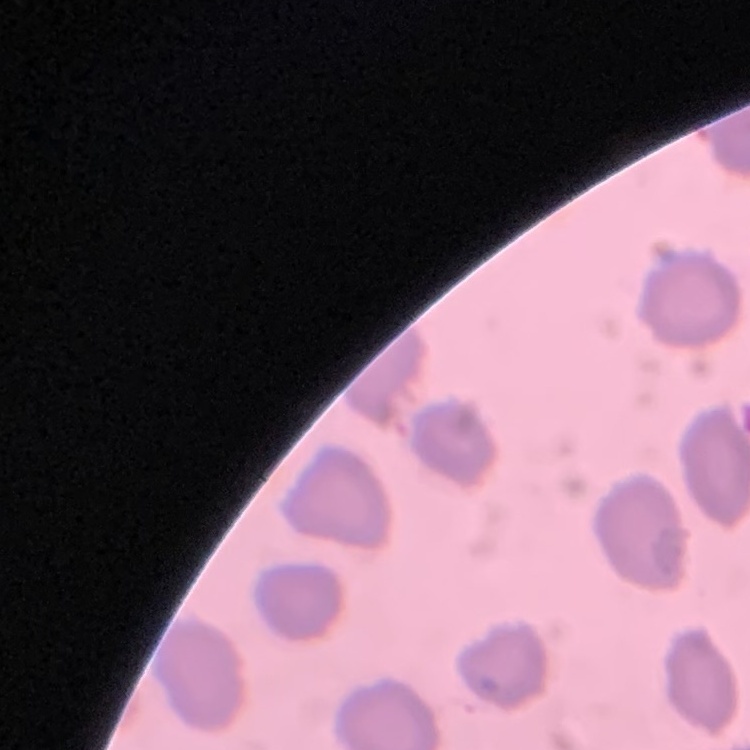
Summary:
  - Red blood cell morphology: no rouleaux formation
  - Preparation: thin peripheral smear
  - Image type: one tile cut from a larger photomicrograph
  - Stain: Field's or Giemsa